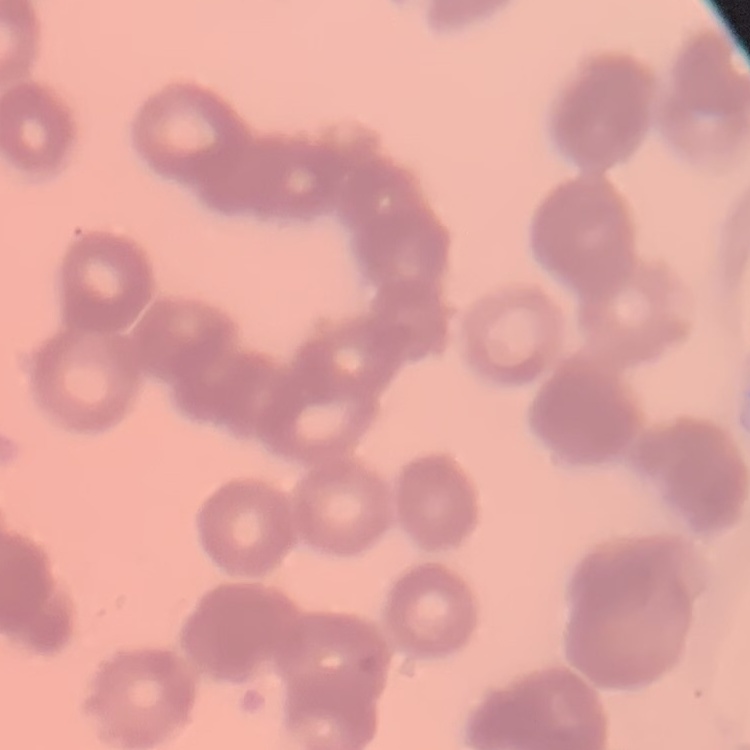

erythrocyte_morphology: rouleaux formation
stain: Field's or Giemsa
image_type: one tile cut from a larger photomicrograph
preparation: thin blood film